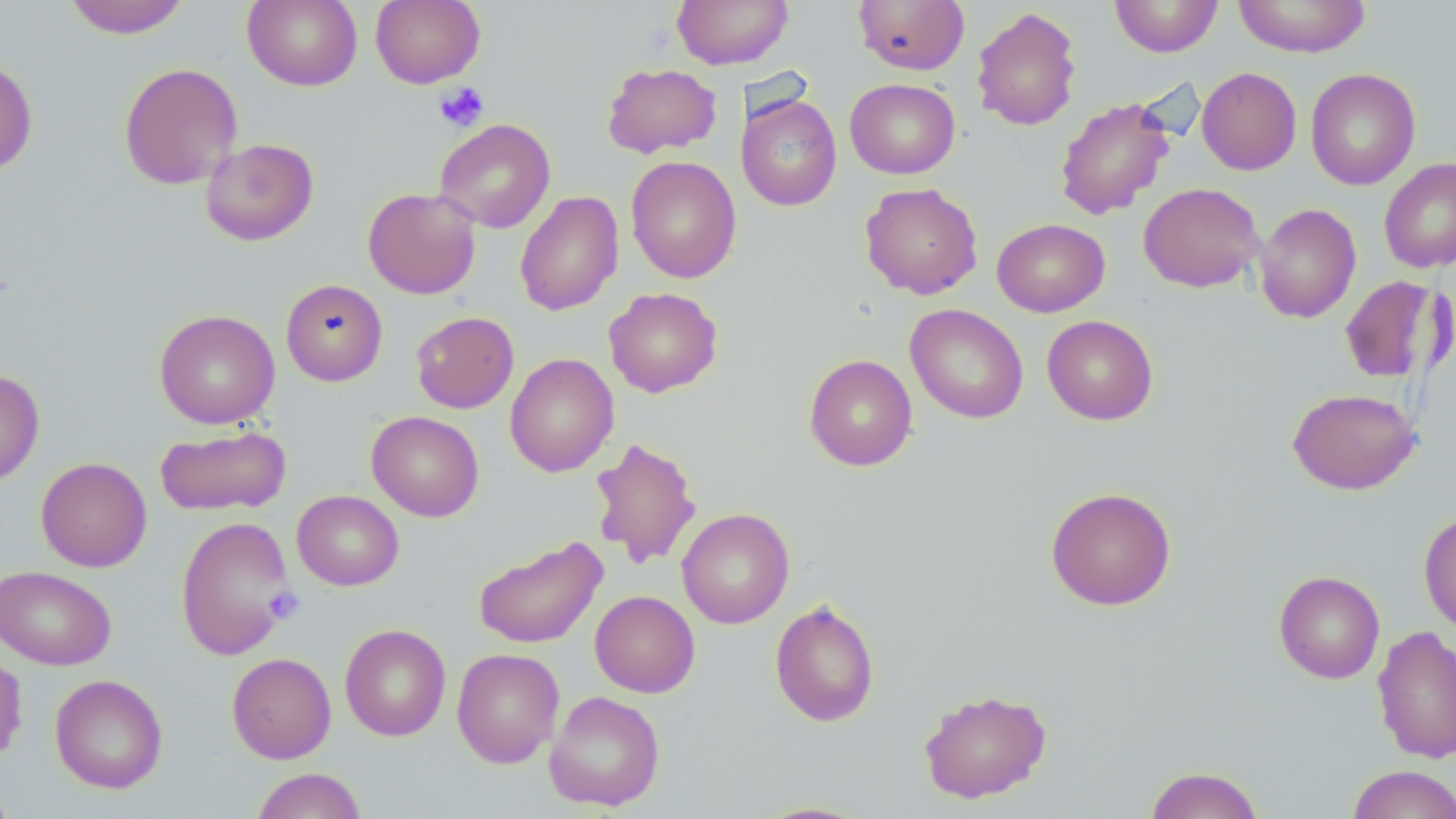

slide-level diagnosis = no evidence of blood parasites
field of view = one of a larger specimen
magnification = 1000x
stain = May-Grünwald-Giemsa
preparation = thin blood film
platelet locations = approximate bounding boxes as (x1, y1, x2, y2) in pixels: (434, 82, 489, 132), (266, 587, 303, 622)
modality = optical microscopy
uninfected red blood cell locations = approximate bounding boxes as (x1, y1, x2, y2) in pixels: (63, 0, 191, 38), (243, 0, 362, 90), (370, 0, 486, 88), (672, 0, 794, 69), (853, 0, 970, 75), (1109, 0, 1223, 57), (1232, 0, 1371, 58), (971, 6, 1082, 131), (0, 57, 38, 177), (118, 62, 242, 189), (602, 62, 722, 159), (1197, 67, 1302, 175), (1305, 68, 1421, 190), (845, 79, 960, 178), (736, 94, 842, 211), (1055, 97, 1175, 220), (434, 118, 555, 233), (201, 138, 319, 246), (626, 156, 741, 283), (1379, 157, 1456, 273), (860, 182, 983, 300), (1138, 183, 1263, 292), (362, 187, 481, 299), (515, 191, 623, 316), (1254, 203, 1361, 323), (992, 218, 1110, 317), (1339, 275, 1446, 384), (280, 279, 388, 386), (604, 287, 723, 398), (905, 304, 1029, 424), (154, 309, 280, 429), (411, 311, 519, 413), (1042, 315, 1158, 425), (504, 353, 619, 477), (804, 354, 918, 471), (0, 369, 44, 487), (1287, 387, 1419, 494), (366, 411, 484, 522), (155, 424, 291, 516), (587, 436, 702, 570), (35, 457, 152, 572), (1045, 486, 1176, 611), (292, 490, 404, 591), (677, 507, 795, 629), (1418, 512, 1456, 636), (175, 515, 295, 660), (472, 536, 608, 649), (0, 564, 116, 670), (1273, 570, 1385, 684), (590, 590, 700, 698), (769, 597, 880, 727), (339, 623, 451, 742), (1373, 625, 1456, 764), (0, 647, 28, 765), (452, 648, 564, 768), (226, 652, 336, 763), (49, 674, 168, 794), (918, 688, 1053, 803), (544, 690, 666, 811), (1346, 765, 1456, 819), (1144, 766, 1265, 819), (251, 768, 366, 819), (0, 780, 17, 818), (749, 800, 876, 818)
image size = 1456×819 pixels